Evaluate for malaria.
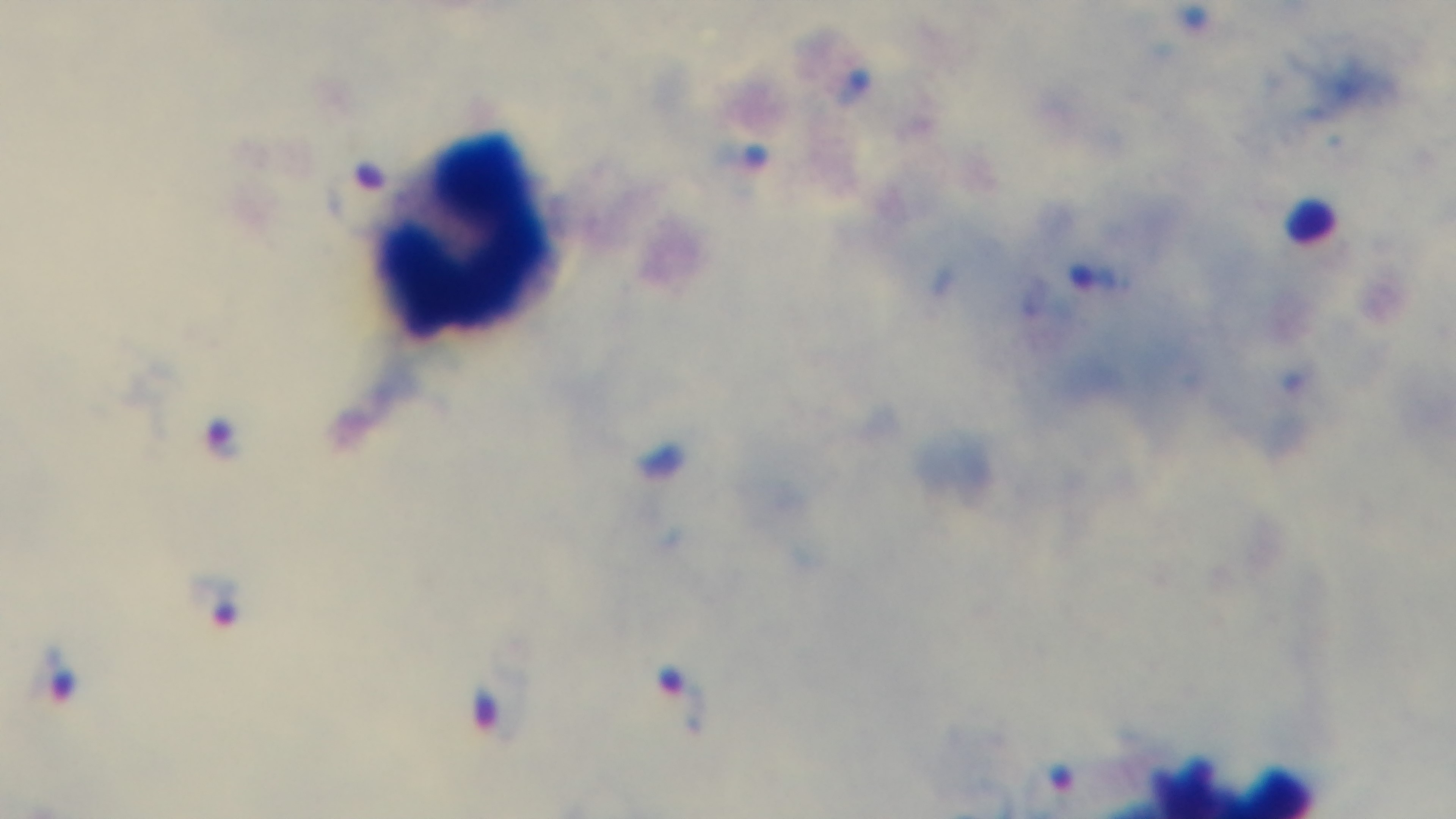
It is infected.

Preparation: thick smear. Giemsa-stained. Oil-immersion objective, 100x. Light microscopy. Captured with a mounted 4K digital camera. Single field of view.